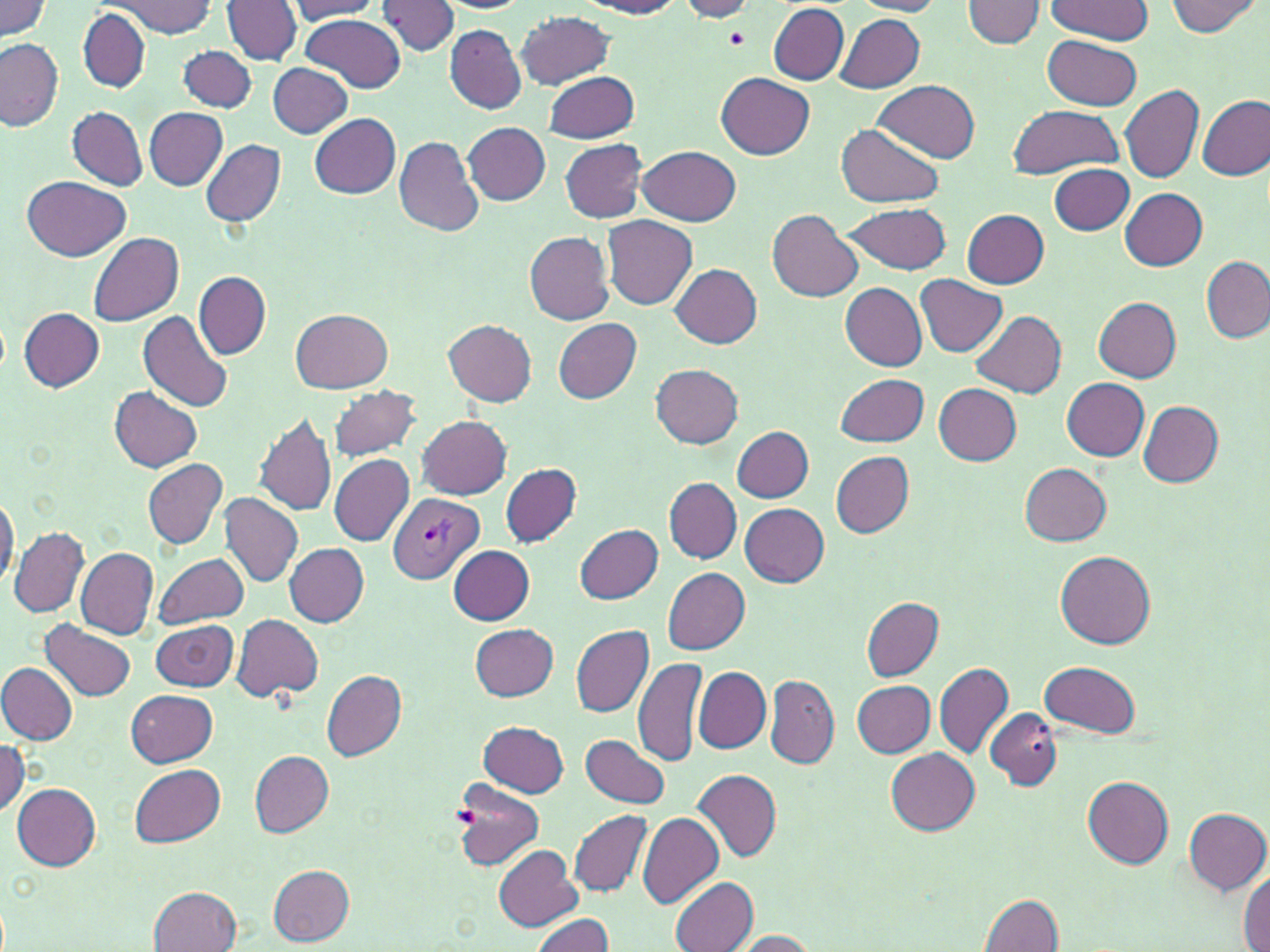
Summary:
  - Coordinate format: approximate bounding boxes as named x1/y1/x2/y2 corners in pixels
  - Platelet locations: (x1=724, y1=28, x2=749, y2=50)
  - Plasmodium vivax-infected red blood cell locations: (x1=389, y1=493, x2=482, y2=582)
  - Uninfected red blood cell locations: (x1=222, y1=0, x2=302, y2=65), (x1=580, y1=0, x2=684, y2=18), (x1=677, y1=0, x2=761, y2=21), (x1=1047, y1=0, x2=1151, y2=44), (x1=1166, y1=0, x2=1261, y2=36), (x1=0, y1=1, x2=54, y2=41), (x1=106, y1=1, x2=217, y2=37), (x1=288, y1=1, x2=382, y2=21), (x1=375, y1=1, x2=459, y2=57), (x1=435, y1=1, x2=531, y2=14), (x1=849, y1=1, x2=946, y2=16), (x1=964, y1=1, x2=1045, y2=48), (x1=767, y1=4, x2=849, y2=84), (x1=79, y1=9, x2=151, y2=93), (x1=516, y1=12, x2=613, y2=90), (x1=301, y1=13, x2=407, y2=93), (x1=836, y1=14, x2=924, y2=92), (x1=444, y1=26, x2=527, y2=112), (x1=1042, y1=34, x2=1142, y2=110), (x1=1, y1=38, x2=63, y2=131), (x1=177, y1=45, x2=256, y2=113), (x1=267, y1=63, x2=353, y2=138), (x1=546, y1=71, x2=638, y2=143), (x1=716, y1=72, x2=815, y2=160), (x1=874, y1=80, x2=980, y2=163), (x1=1120, y1=85, x2=1204, y2=183), (x1=1198, y1=93, x2=1270, y2=181), (x1=1007, y1=104, x2=1122, y2=179), (x1=67, y1=106, x2=147, y2=190), (x1=144, y1=107, x2=227, y2=191), (x1=310, y1=114, x2=401, y2=199), (x1=462, y1=122, x2=552, y2=204), (x1=836, y1=124, x2=943, y2=208), (x1=395, y1=136, x2=484, y2=238), (x1=202, y1=139, x2=286, y2=228), (x1=560, y1=140, x2=647, y2=222), (x1=638, y1=145, x2=741, y2=226), (x1=1048, y1=164, x2=1135, y2=234), (x1=22, y1=175, x2=130, y2=262), (x1=1121, y1=188, x2=1207, y2=271), (x1=842, y1=203, x2=953, y2=274), (x1=961, y1=209, x2=1050, y2=289), (x1=768, y1=210, x2=864, y2=303), (x1=602, y1=215, x2=697, y2=309), (x1=524, y1=232, x2=615, y2=325), (x1=88, y1=233, x2=184, y2=326), (x1=1201, y1=254, x2=1270, y2=343), (x1=671, y1=263, x2=763, y2=348), (x1=194, y1=271, x2=269, y2=358), (x1=916, y1=274, x2=1007, y2=356), (x1=841, y1=282, x2=926, y2=371), (x1=1094, y1=297, x2=1182, y2=381), (x1=20, y1=307, x2=103, y2=391), (x1=139, y1=310, x2=233, y2=412), (x1=290, y1=310, x2=394, y2=393), (x1=970, y1=310, x2=1067, y2=396), (x1=553, y1=318, x2=642, y2=403), (x1=444, y1=319, x2=537, y2=406), (x1=651, y1=364, x2=743, y2=449), (x1=835, y1=373, x2=928, y2=445), (x1=1062, y1=378, x2=1150, y2=461), (x1=327, y1=384, x2=422, y2=462), (x1=933, y1=384, x2=1022, y2=465), (x1=112, y1=386, x2=202, y2=472), (x1=1138, y1=401, x2=1224, y2=486), (x1=254, y1=413, x2=337, y2=517), (x1=418, y1=416, x2=512, y2=499), (x1=732, y1=426, x2=814, y2=501), (x1=830, y1=452, x2=914, y2=538), (x1=329, y1=455, x2=413, y2=546), (x1=144, y1=458, x2=227, y2=549), (x1=500, y1=463, x2=581, y2=547), (x1=1020, y1=463, x2=1113, y2=546), (x1=664, y1=478, x2=742, y2=562), (x1=0, y1=494, x2=18, y2=589), (x1=219, y1=494, x2=303, y2=589), (x1=740, y1=503, x2=829, y2=587), (x1=574, y1=523, x2=662, y2=602), (x1=10, y1=526, x2=87, y2=618), (x1=283, y1=542, x2=368, y2=626), (x1=449, y1=546, x2=534, y2=624), (x1=75, y1=548, x2=158, y2=640), (x1=1056, y1=549, x2=1155, y2=648), (x1=154, y1=553, x2=249, y2=628), (x1=662, y1=567, x2=750, y2=654), (x1=861, y1=597, x2=943, y2=680), (x1=231, y1=614, x2=324, y2=703), (x1=150, y1=619, x2=239, y2=692), (x1=42, y1=620, x2=134, y2=701), (x1=469, y1=623, x2=559, y2=701), (x1=571, y1=624, x2=653, y2=718), (x1=633, y1=656, x2=708, y2=767), (x1=1040, y1=660, x2=1141, y2=737), (x1=933, y1=661, x2=1014, y2=758), (x1=0, y1=662, x2=77, y2=745), (x1=694, y1=667, x2=771, y2=753), (x1=322, y1=670, x2=406, y2=760), (x1=764, y1=674, x2=839, y2=769), (x1=853, y1=680, x2=935, y2=756), (x1=125, y1=689, x2=217, y2=766), (x1=986, y1=708, x2=1061, y2=790), (x1=479, y1=722, x2=569, y2=797), (x1=582, y1=734, x2=669, y2=808), (x1=0, y1=737, x2=27, y2=815), (x1=885, y1=747, x2=980, y2=832), (x1=249, y1=751, x2=333, y2=836), (x1=131, y1=764, x2=226, y2=846), (x1=693, y1=769, x2=781, y2=862), (x1=1082, y1=777, x2=1175, y2=868), (x1=451, y1=778, x2=545, y2=872), (x1=12, y1=784, x2=102, y2=871), (x1=1184, y1=808, x2=1270, y2=894), (x1=569, y1=810, x2=652, y2=896), (x1=637, y1=812, x2=724, y2=909), (x1=494, y1=844, x2=581, y2=931), (x1=267, y1=862, x2=356, y2=945), (x1=1240, y1=870, x2=1270, y2=952), (x1=669, y1=876, x2=756, y2=952), (x1=149, y1=886, x2=242, y2=952), (x1=979, y1=893, x2=1065, y2=952), (x1=529, y1=913, x2=616, y2=952), (x1=728, y1=930, x2=818, y2=951)
  - Slide-level diagnosis: Plasmodium vivax
  - Field of view: one of a larger specimen
  - Stain: May-Grünwald-Giemsa
  - Magnification: 1000x
  - Image size: 1270×952 pixels
  - Modality: light microscopy
  - Preparation: thin blood smear